Assess this cell for malaria.
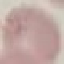
Uninfected.

Photographed with a smartphone camera at the microscope eyepiece. Automatically extracted cell patch, resized to 64 × 64 pixels. Giemsa stain. Thin blood film.